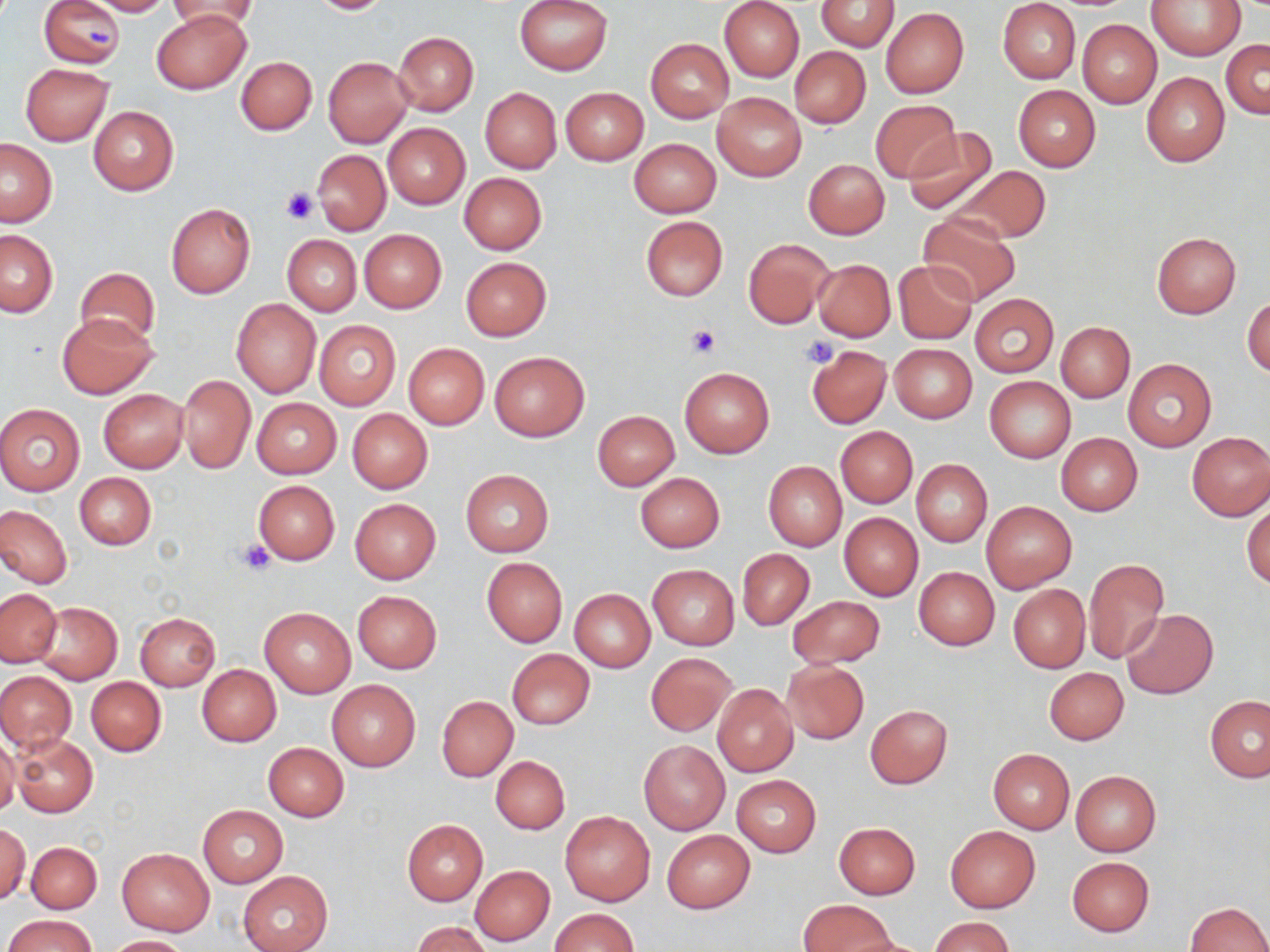

Approximate bounding boxes as named x1/y1/x2/y2 corners in pixels. Uninfected red blood cell locations: (x1=89, y1=0, x2=173, y2=16), (x1=168, y1=0, x2=258, y2=34), (x1=306, y1=0, x2=397, y2=15), (x1=514, y1=0, x2=612, y2=76), (x1=721, y1=0, x2=804, y2=82), (x1=816, y1=0, x2=900, y2=51), (x1=1147, y1=0, x2=1245, y2=59), (x1=40, y1=1, x2=124, y2=67), (x1=997, y1=1, x2=1081, y2=83), (x1=880, y1=7, x2=968, y2=98), (x1=152, y1=8, x2=252, y2=95), (x1=1077, y1=20, x2=1161, y2=109), (x1=393, y1=32, x2=479, y2=115), (x1=645, y1=39, x2=734, y2=124), (x1=1222, y1=40, x2=1269, y2=118), (x1=790, y1=46, x2=869, y2=128), (x1=236, y1=56, x2=317, y2=134), (x1=323, y1=56, x2=414, y2=148), (x1=20, y1=63, x2=113, y2=146), (x1=1141, y1=72, x2=1230, y2=167), (x1=1013, y1=85, x2=1100, y2=172), (x1=480, y1=87, x2=561, y2=173), (x1=561, y1=87, x2=648, y2=165), (x1=712, y1=92, x2=806, y2=181), (x1=870, y1=100, x2=960, y2=181), (x1=88, y1=105, x2=178, y2=196), (x1=382, y1=123, x2=470, y2=209), (x1=903, y1=127, x2=997, y2=214), (x1=0, y1=138, x2=57, y2=226), (x1=629, y1=139, x2=721, y2=217), (x1=313, y1=150, x2=390, y2=235), (x1=803, y1=159, x2=889, y2=239), (x1=954, y1=165, x2=1051, y2=245), (x1=459, y1=172, x2=546, y2=254), (x1=166, y1=204, x2=255, y2=299), (x1=918, y1=213, x2=1019, y2=305), (x1=640, y1=216, x2=727, y2=300), (x1=360, y1=229, x2=446, y2=313), (x1=0, y1=230, x2=57, y2=317), (x1=1151, y1=232, x2=1239, y2=317), (x1=282, y1=234, x2=361, y2=316), (x1=743, y1=239, x2=832, y2=328), (x1=461, y1=258, x2=551, y2=341), (x1=894, y1=259, x2=978, y2=344), (x1=813, y1=260, x2=895, y2=341), (x1=75, y1=268, x2=158, y2=347), (x1=971, y1=295, x2=1058, y2=376), (x1=1244, y1=296, x2=1270, y2=378), (x1=231, y1=299, x2=321, y2=399), (x1=55, y1=312, x2=158, y2=399), (x1=314, y1=321, x2=401, y2=411), (x1=1056, y1=321, x2=1135, y2=402), (x1=403, y1=343, x2=489, y2=430), (x1=806, y1=344, x2=890, y2=427), (x1=889, y1=344, x2=977, y2=422), (x1=489, y1=351, x2=589, y2=441), (x1=1123, y1=359, x2=1217, y2=452), (x1=679, y1=367, x2=774, y2=457), (x1=177, y1=375, x2=255, y2=474), (x1=984, y1=375, x2=1076, y2=463), (x1=98, y1=389, x2=188, y2=472), (x1=252, y1=399, x2=340, y2=478), (x1=0, y1=403, x2=85, y2=496), (x1=347, y1=408, x2=433, y2=493), (x1=593, y1=410, x2=680, y2=490), (x1=836, y1=427, x2=917, y2=507), (x1=1186, y1=432, x2=1270, y2=520), (x1=1056, y1=433, x2=1143, y2=516), (x1=910, y1=459, x2=992, y2=547), (x1=763, y1=462, x2=847, y2=550), (x1=461, y1=469, x2=553, y2=556), (x1=74, y1=472, x2=156, y2=549), (x1=635, y1=472, x2=724, y2=552), (x1=253, y1=480, x2=340, y2=565), (x1=349, y1=498, x2=440, y2=583), (x1=1243, y1=498, x2=1270, y2=589), (x1=982, y1=500, x2=1076, y2=592), (x1=0, y1=504, x2=72, y2=587), (x1=839, y1=513, x2=922, y2=601), (x1=737, y1=549, x2=814, y2=630), (x1=482, y1=558, x2=567, y2=646), (x1=1084, y1=558, x2=1169, y2=663), (x1=648, y1=566, x2=739, y2=649), (x1=914, y1=566, x2=999, y2=650), (x1=1008, y1=584, x2=1090, y2=673), (x1=1, y1=588, x2=61, y2=667), (x1=569, y1=589, x2=655, y2=671), (x1=353, y1=591, x2=442, y2=673), (x1=788, y1=596, x2=884, y2=667), (x1=31, y1=601, x2=122, y2=685), (x1=260, y1=606, x2=356, y2=698), (x1=1121, y1=609, x2=1218, y2=699), (x1=135, y1=613, x2=220, y2=691), (x1=506, y1=649, x2=595, y2=729), (x1=645, y1=653, x2=737, y2=736), (x1=782, y1=661, x2=869, y2=744), (x1=196, y1=664, x2=281, y2=746), (x1=1043, y1=666, x2=1128, y2=744), (x1=0, y1=670, x2=76, y2=752), (x1=86, y1=677, x2=166, y2=756), (x1=326, y1=679, x2=422, y2=771), (x1=712, y1=684, x2=798, y2=778), (x1=437, y1=695, x2=518, y2=782), (x1=1206, y1=695, x2=1270, y2=781), (x1=866, y1=704, x2=952, y2=788), (x1=10, y1=733, x2=97, y2=818), (x1=0, y1=737, x2=20, y2=818), (x1=639, y1=741, x2=730, y2=835), (x1=264, y1=742, x2=349, y2=821), (x1=987, y1=749, x2=1075, y2=833), (x1=490, y1=756, x2=569, y2=833), (x1=1070, y1=770, x2=1160, y2=857), (x1=732, y1=775, x2=821, y2=856), (x1=198, y1=805, x2=286, y2=887), (x1=560, y1=812, x2=655, y2=907), (x1=402, y1=820, x2=488, y2=904), (x1=1, y1=822, x2=31, y2=906), (x1=834, y1=822, x2=920, y2=898), (x1=945, y1=826, x2=1041, y2=912), (x1=662, y1=830, x2=755, y2=913), (x1=26, y1=841, x2=102, y2=914), (x1=116, y1=848, x2=215, y2=936), (x1=1067, y1=856, x2=1154, y2=937), (x1=470, y1=865, x2=555, y2=945), (x1=238, y1=872, x2=332, y2=952), (x1=799, y1=899, x2=895, y2=951), (x1=1186, y1=902, x2=1270, y2=952), (x1=550, y1=908, x2=639, y2=952), (x1=5, y1=914, x2=96, y2=952), (x1=931, y1=916, x2=1014, y2=952), (x1=411, y1=921, x2=492, y2=952), (x1=107, y1=935, x2=191, y2=952). Platelet locations: (x1=86, y1=23, x2=114, y2=50), (x1=281, y1=187, x2=319, y2=224), (x1=685, y1=325, x2=720, y2=359), (x1=801, y1=334, x2=839, y2=369), (x1=234, y1=539, x2=277, y2=574). Slide-level diagnosis: negative for blood parasites. Light microscopy. Thin blood film. Image is 1270×952 pixels. Single field of view. May-Grünwald-Giemsa-stained preparation. Captured at 1000x magnification.